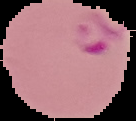

Malaria status: parasitized. Image is 136×121 pixels. From a thin blood smear. Cell region segmented out of the field of view; the surrounding area is masked to black.